Comment on the morphology of the red blood cells.
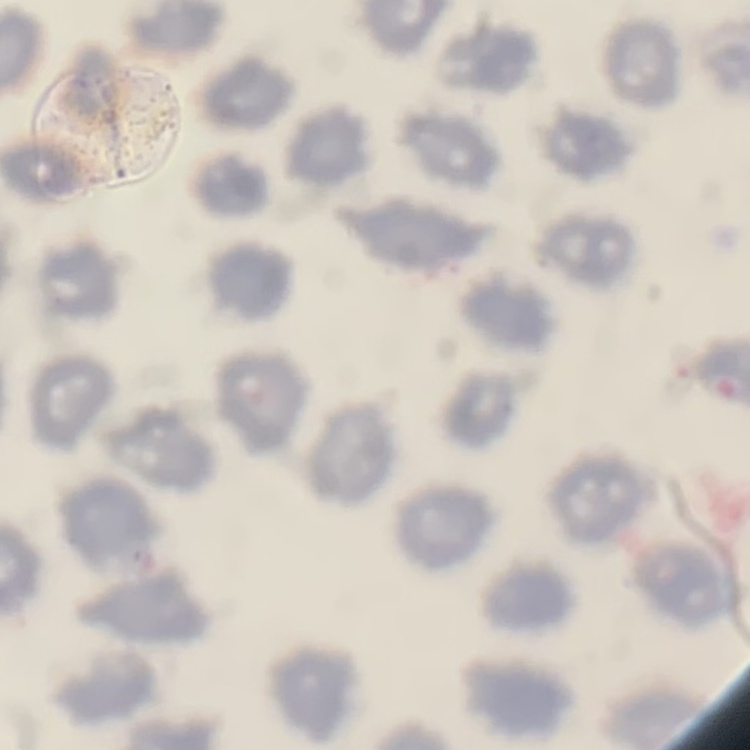
No rouleaux formation.

Stained with either Field's or Giemsa. One tile cut from a larger photomicrograph. Thin blood film.